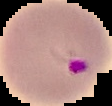 Image is 112×106 pixels. Result: malaria parasites identified. From a thin blood film. Segmented cell region on a black background.